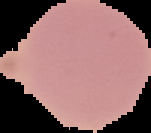

Summary:
  - Image size: 151×133 pixels
  - Result: no Plasmodium parasites detected
  - Preparation: thin blood film
  - Image type: segmented cell region with the area outside set to black